Give the position of every Plasmodium parasite and every leukocyte.
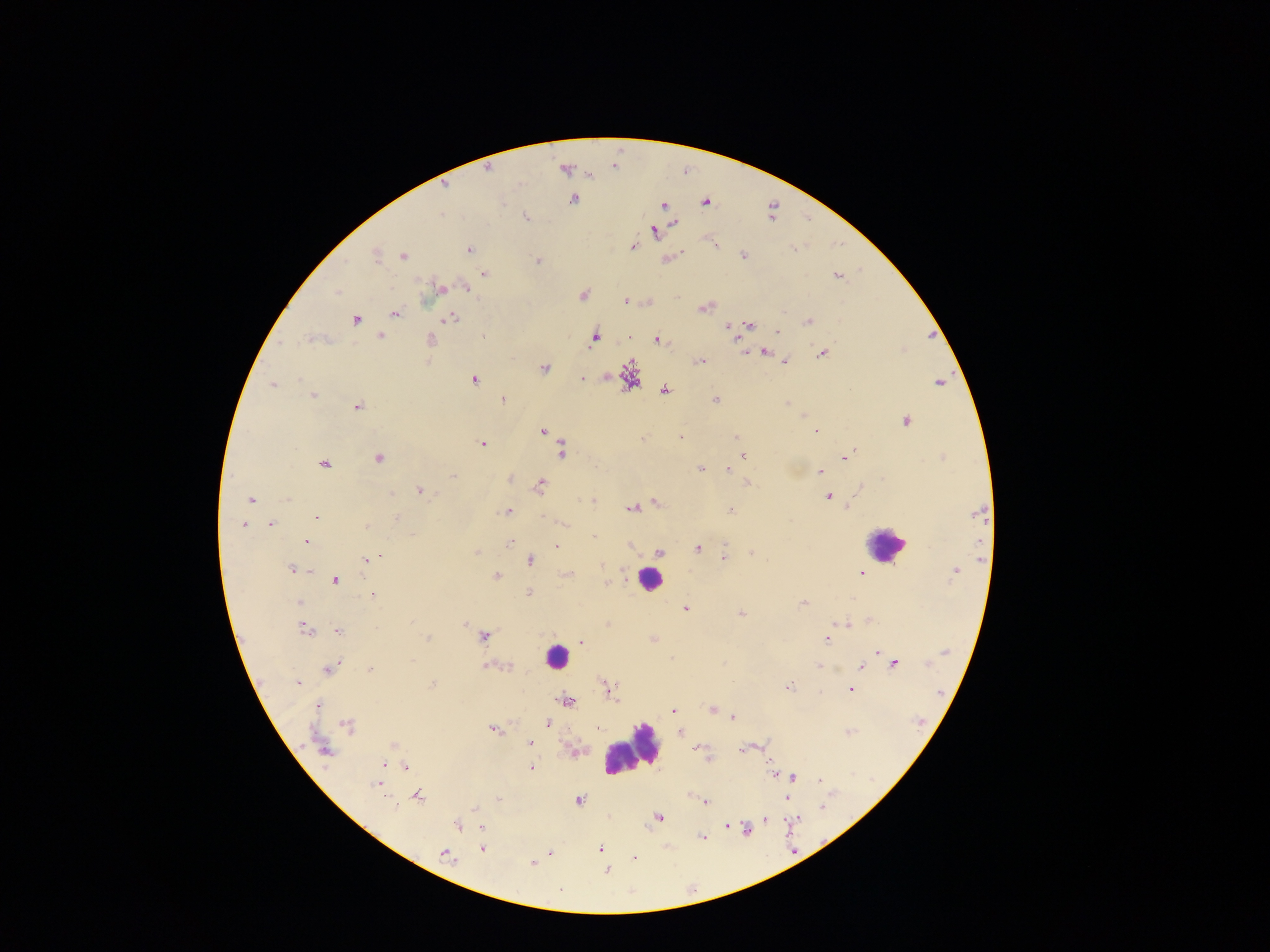

Approximate centers as x y in pixels.
Plasmodium parasites: 487 167; 563 171; 447 188; 574 201; 705 201; 702 205; 662 207; 440 215; 527 218; 674 224; 655 232; 631 247; 469 248; 742 256; 375 257; 402 257; 537 259; 484 273; 836 276; 464 287; 442 290; 338 291; 581 294; 625 299; 702 309; 394 313; 782 313; 450 318; 808 321; 357 322; 749 327; 725 328; 779 331; 731 334; 595 335; 381 336; 656 338; 308 339; 431 341; 737 344; 742 351; 766 351; 821 354; 428 360; 784 360; 700 361; 545 370; 581 376; 300 378; 473 380; 940 383; 272 386; 665 390; 313 393; 503 399; 715 401; 788 403; 356 407; 803 416; 904 421; 544 431; 815 431; 680 436; 735 437; 643 439; 483 445; 561 449; 852 451; 742 454; 848 455; 378 458; 325 467; 701 468; 818 470; 727 471; 453 477; 511 479; 748 483; 541 486; 860 488; 419 489; 390 495; 829 497; 251 500; 592 501; 656 501; 847 505; 631 508; 731 510; 508 512; 542 516; 316 519; 395 519; 271 524; 562 525; 244 526; 368 527; 593 536; 306 543; 510 543; 558 547; 697 549; 658 551; 751 551; 477 552; 724 557; 372 559; 529 560; 366 561; 600 565; 292 568; 310 570; 955 571; 605 573; 496 574; 567 574; 862 574; 337 580; 609 582; 529 592; 374 595; 299 602; 802 602; 686 609; 739 613; 836 623; 843 623; 465 624; 305 629; 337 631; 427 637; 484 637; 582 641; 826 641; 877 652; 944 654; 411 662; 336 663; 895 664; 926 664; 817 665; 507 666; 331 667; 488 667; 859 667; 369 668; 837 668; 297 684; 433 684; 789 687; 850 689; 564 701; 320 705; 672 709; 710 709; 733 718; 548 724; 347 726; 598 727; 490 728; 679 732; 849 734; 528 741; 393 744; 741 748; 696 750; 325 752; 708 759; 386 762; 532 766; 406 768; 770 773; 793 777; 819 781; 375 784; 419 795; 497 798; 787 798; 579 800; 705 804; 475 808; 659 817; 766 819; 726 824; 458 825; 481 829; 599 849; 481 850; 443 854; 634 858; 531 864; 607 869; 559 891.
Leukocytes: 888 543; 649 579; 555 656; 629 747.

capture: mobile-phone photograph through a microscope
field_of_view: single
country: Ghana
preparation: thick blood film
image_size: 1270×952 pixels